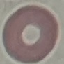

Summary:
  - Malaria status: uninfected
  - Preparation: thin smear
  - Image type: automatically extracted cell patch, resized to 64 × 64 pixels
  - Capture: smartphone camera at the microscope eyepiece
  - Stain: Giemsa